Locate every Plasmodium malariae-infected red blood cell.
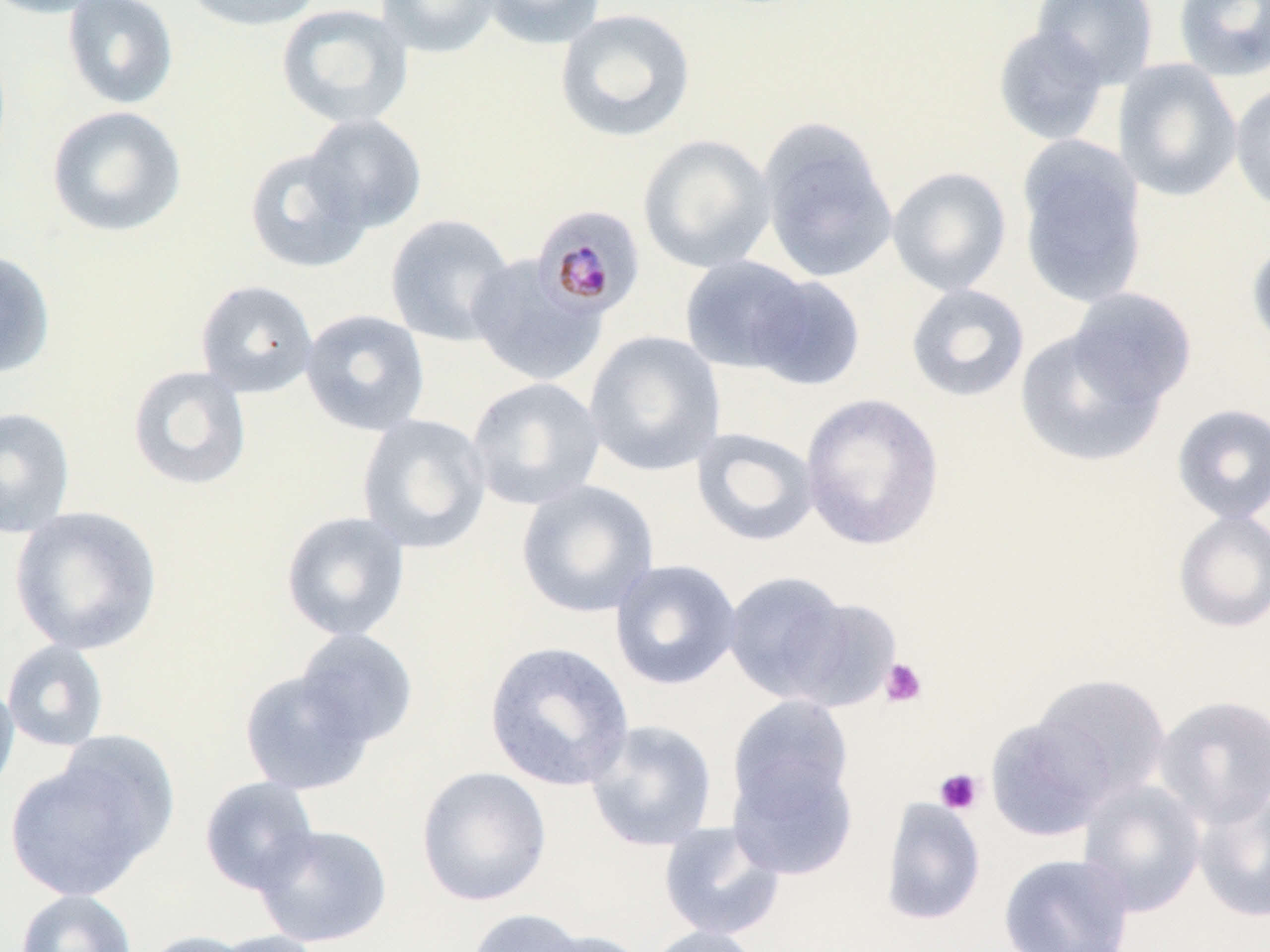
Approximate bounding boxes as [x1, y1, x2, y2] in pixels.
Plasmodium malariae-infected red blood cells: [533, 205, 646, 318].

{
  "slide_level_diagnosis": "Plasmodium malariae",
  "uninfected_red_blood_cell_locations": "approximate bounding boxes as [x1, y1, x2, y2] in pixels: [0, 0, 110, 19], [62, 0, 179, 110], [181, 0, 324, 32], [375, 0, 503, 58], [480, 0, 608, 50], [1032, 0, 1159, 88], [1173, 0, 1270, 81], [276, 3, 413, 130], [555, 8, 696, 143], [992, 25, 1111, 146], [1114, 59, 1243, 202], [1229, 81, 1270, 215], [46, 105, 187, 237], [302, 112, 428, 233], [758, 118, 898, 284], [638, 134, 776, 274], [1016, 139, 1148, 308], [243, 147, 372, 274], [886, 166, 1012, 296], [384, 214, 517, 347], [1247, 237, 1270, 352], [0, 250, 56, 379], [467, 254, 607, 387], [680, 255, 814, 375], [745, 273, 867, 391], [195, 279, 319, 398], [905, 283, 1030, 403], [1066, 288, 1197, 409], [300, 308, 431, 437], [1014, 327, 1166, 468], [584, 330, 726, 476], [126, 364, 253, 491], [466, 376, 606, 510], [799, 393, 945, 549], [1171, 403, 1270, 524], [0, 406, 76, 538], [356, 413, 492, 554], [691, 427, 820, 548], [515, 479, 660, 619], [10, 506, 163, 655], [1172, 509, 1270, 633], [280, 510, 411, 642], [609, 559, 742, 691], [723, 570, 855, 704], [781, 596, 902, 713], [294, 628, 419, 748], [1, 639, 111, 752], [484, 641, 635, 792], [238, 668, 376, 796], [1031, 673, 1172, 803], [0, 675, 19, 802], [727, 694, 855, 823], [1153, 694, 1270, 829], [984, 715, 1114, 842], [584, 719, 718, 852], [727, 752, 858, 879], [3, 755, 164, 902], [415, 765, 552, 907], [199, 776, 320, 895], [1077, 779, 1206, 917], [1193, 787, 1270, 923], [879, 796, 986, 926], [657, 820, 787, 942], [253, 822, 393, 948], [997, 853, 1136, 952], [15, 889, 138, 952], [465, 907, 592, 952], [642, 925, 767, 952], [529, 929, 652, 952], [137, 930, 259, 952], [206, 930, 330, 952]",
  "magnification": "1000x",
  "preparation": "thin blood smear",
  "stain": "May-Grünwald-Giemsa",
  "image_size": "1270×952 pixels",
  "field_of_view": "one of a larger specimen",
  "platelet_locations": "approximate bounding boxes as [x1, y1, x2, y2] in pixels: [880, 657, 928, 707], [934, 768, 984, 815]",
  "modality": "optical microscopy"
}